Name the blood parasite species.
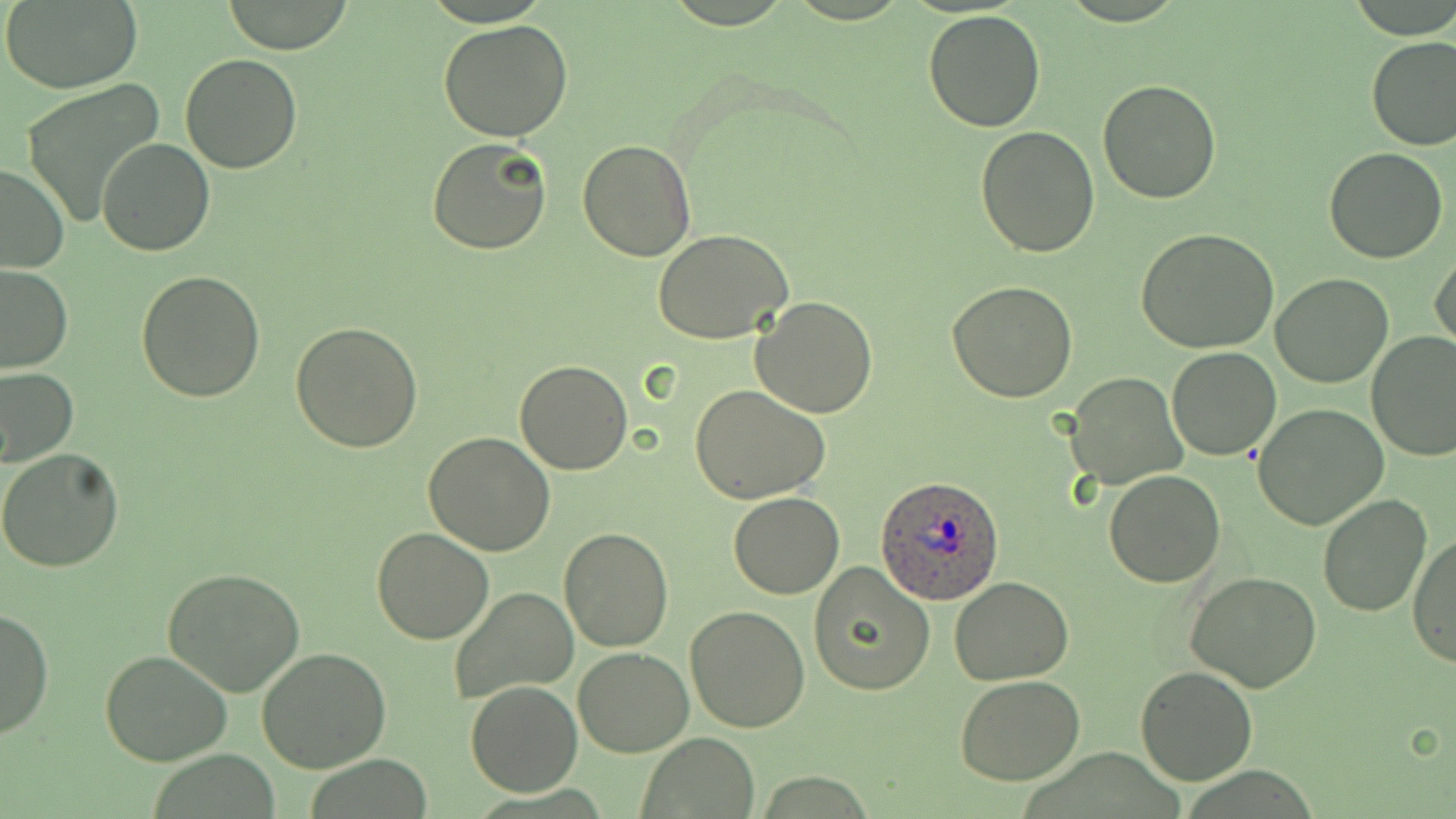
Plasmodium ovale.

Summary:
  - Coordinate format: approximate bounding boxes as (x1, y1, x2, y2) in pixels
  - Plasmodium ovale-infected red blood cell locations: (875, 476, 1004, 604)
  - Uninfected red blood cell locations: (2, 1, 143, 92), (219, 1, 355, 53), (922, 9, 1048, 131), (438, 19, 574, 140), (1365, 34, 1456, 151), (179, 53, 305, 174), (19, 78, 166, 229), (1097, 80, 1222, 204), (975, 126, 1100, 257), (427, 136, 552, 256), (97, 139, 215, 257), (577, 139, 699, 262), (1324, 148, 1448, 263), (0, 161, 68, 274), (1136, 229, 1281, 354), (654, 230, 793, 343), (1432, 248, 1456, 354), (0, 265, 73, 374), (135, 270, 265, 403), (1270, 273, 1394, 388), (947, 282, 1078, 403), (750, 297, 879, 419), (290, 319, 424, 452), (1366, 330, 1456, 461), (1166, 346, 1282, 461), (514, 358, 633, 475), (0, 365, 78, 467), (1066, 374, 1187, 492), (689, 383, 832, 504), (1252, 403, 1389, 532), (423, 432, 555, 555), (0, 448, 125, 573), (1103, 470, 1225, 588), (728, 493, 845, 599), (1316, 493, 1431, 617), (370, 526, 493, 644), (558, 528, 675, 651), (1409, 531, 1455, 670), (807, 562, 935, 697), (162, 567, 305, 697), (1184, 571, 1323, 693), (950, 577, 1074, 685), (448, 587, 578, 702), (685, 605, 813, 734), (0, 606, 53, 741), (574, 647, 693, 757), (255, 648, 391, 774), (101, 649, 233, 767), (1134, 665, 1257, 785), (954, 676, 1085, 785), (465, 681, 582, 797), (639, 734, 760, 818)
  - Modality: light microscopy
  - Magnification: 1000x
  - Stain: May-Grünwald-Giemsa
  - Image size: 1456×819 pixels
  - Preparation: thin blood film
  - Field of view: one of a larger specimen